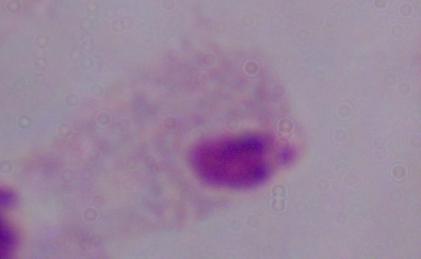

{
  "identification": "trichomonad",
  "magnification": "1000x",
  "modality": "micrograph"
}